Classify this cell by malaria status.
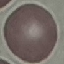

Uninfected.

Thin blood film. Automatically extracted cell patch, resized to 64 × 64 pixels. Giemsa-stained preparation. Photographed with a smartphone camera at the microscope eyepiece.